Evaluate for malaria.
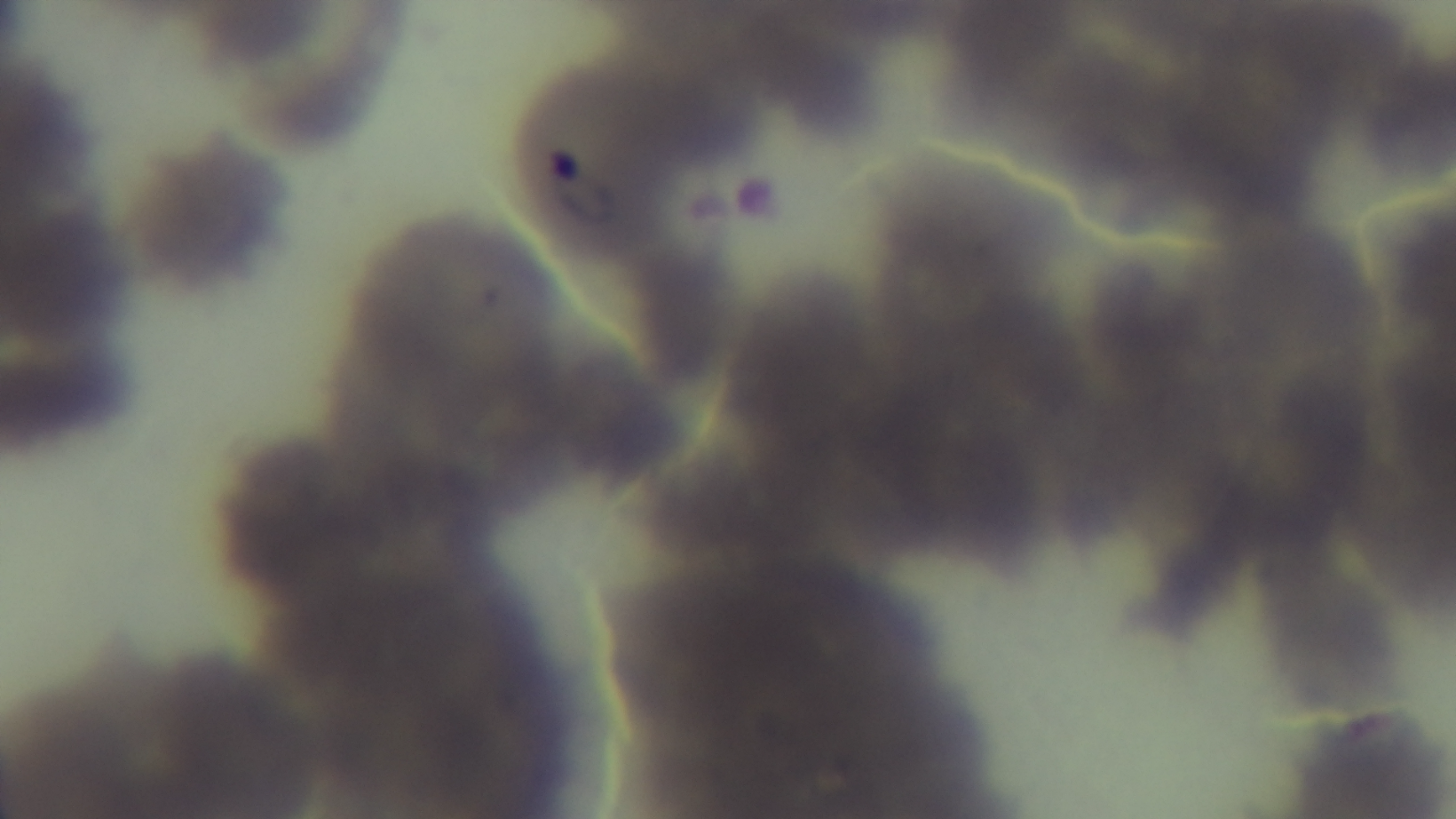
Infected.

Summary:
  - Capture: mounted 4K digital camera
  - Modality: light microscopy
  - Stain: Giemsa
  - Objective: 100x oil immersion
  - Preparation: thin smear
  - Field of view: one from the slide